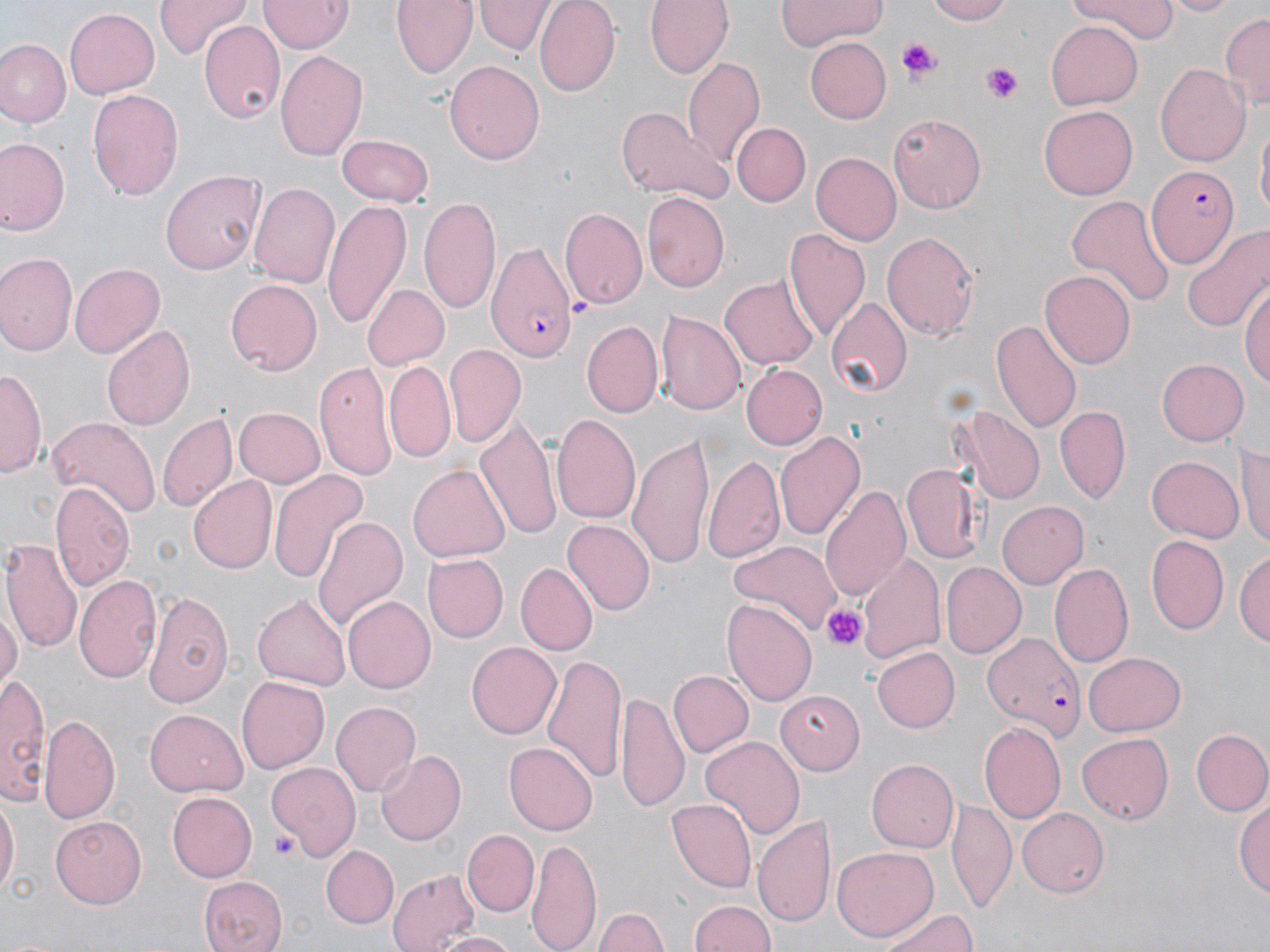

slide-level diagnosis = Plasmodium falciparum
magnification = 1000x
stain = May-Grünwald-Giemsa
modality = optical microscopy
platelet locations = approximate bounding boxes as (x1,y1)-(x2,y2) corner pairs in pixels: (896,36)-(941,84), (983,63)-(1024,104), (824,603)-(868,650), (267,831)-(298,858)
preparation = thin blood smear
field of view = one of a larger specimen
image size = 1270×952 pixels
uninfected red blood cell locations = approximate bounding boxes as (x1,y1)-(x2,y2) corner pairs in pixels: (155,0)-(252,59), (259,0)-(351,54), (393,0)-(478,79), (535,0)-(619,95), (646,0)-(733,78), (774,0)-(887,50), (923,0)-(1012,25), (1065,0)-(1176,40), (1160,0)-(1238,16), (476,1)-(553,55), (63,6)-(157,100), (1220,12)-(1269,112), (200,21)-(285,126), (1046,23)-(1143,110), (804,36)-(892,123), (1,40)-(68,127), (276,48)-(369,165), (681,53)-(766,168), (444,60)-(546,165), (1154,63)-(1251,167), (86,84)-(183,199), (1038,105)-(1135,200), (615,106)-(729,203), (889,109)-(988,210), (1255,118)-(1269,228), (734,125)-(809,206), (336,136)-(435,205), (1,139)-(69,235), (813,151)-(905,244), (162,171)-(265,275), (248,180)-(340,291), (642,192)-(731,292), (1065,195)-(1174,309), (419,196)-(500,316), (324,199)-(411,327), (560,208)-(647,307), (1184,221)-(1270,334), (784,228)-(870,339), (881,230)-(981,341), (0,253)-(77,355), (70,262)-(164,360), (1041,270)-(1136,369), (720,273)-(820,368), (225,279)-(322,375), (1241,280)-(1269,392), (360,283)-(449,372), (824,297)-(911,398), (654,308)-(745,416), (993,318)-(1083,436), (102,322)-(196,435), (582,322)-(663,418), (444,342)-(527,447), (315,358)-(400,482), (1156,359)-(1249,446), (384,361)-(456,462), (740,364)-(827,450), (2,367)-(43,479), (953,403)-(1046,505), (1055,405)-(1131,504), (233,406)-(326,488), (157,411)-(237,514), (476,413)-(562,540), (551,413)-(642,529), (45,415)-(157,523), (774,431)-(868,545), (626,432)-(716,573), (1236,443)-(1270,549), (1147,454)-(1244,542), (705,455)-(783,562), (900,462)-(984,564), (409,465)-(509,562), (267,469)-(370,583), (187,475)-(276,573), (51,482)-(134,594), (822,483)-(911,604), (998,502)-(1088,588), (312,516)-(404,633), (564,520)-(654,616), (1145,534)-(1229,636), (1,536)-(83,659), (729,540)-(843,638), (1236,547)-(1270,652), (423,553)-(508,643), (859,553)-(947,668), (518,561)-(598,655), (1048,561)-(1134,669), (941,562)-(1027,659), (74,574)-(163,685), (142,589)-(234,707), (253,593)-(351,689), (342,595)-(436,694), (722,596)-(816,705), (0,597)-(20,698), (466,641)-(562,739), (540,647)-(627,788), (871,647)-(960,733), (1083,651)-(1186,735), (667,671)-(752,757), (1,673)-(52,809), (235,675)-(329,775), (616,691)-(689,810), (774,691)-(863,773), (329,701)-(420,797), (145,709)-(246,795), (40,712)-(119,822), (979,720)-(1067,826), (1190,728)-(1270,817), (1077,733)-(1174,822), (700,734)-(804,840), (503,743)-(596,835), (376,749)-(466,844), (866,758)-(958,854), (265,760)-(360,863), (167,792)-(257,882), (0,793)-(18,901), (1235,795)-(1270,904), (946,797)-(1015,915), (666,799)-(755,891), (1019,807)-(1110,898), (754,814)-(837,927), (50,816)-(148,907), (464,830)-(539,916), (528,838)-(603,952), (320,844)-(398,929), (833,845)-(936,940), (388,867)-(479,952), (199,875)-(288,952), (690,898)-(779,952), (594,905)-(668,952), (876,906)-(983,951), (432,932)-(519,952)
Plasmodium falciparum-infected red blood cell locations = approximate bounding boxes as (x1,y1)-(x2,y2) corner pairs in pixels: (1148,165)-(1237,270), (488,244)-(578,361), (982,633)-(1087,742)